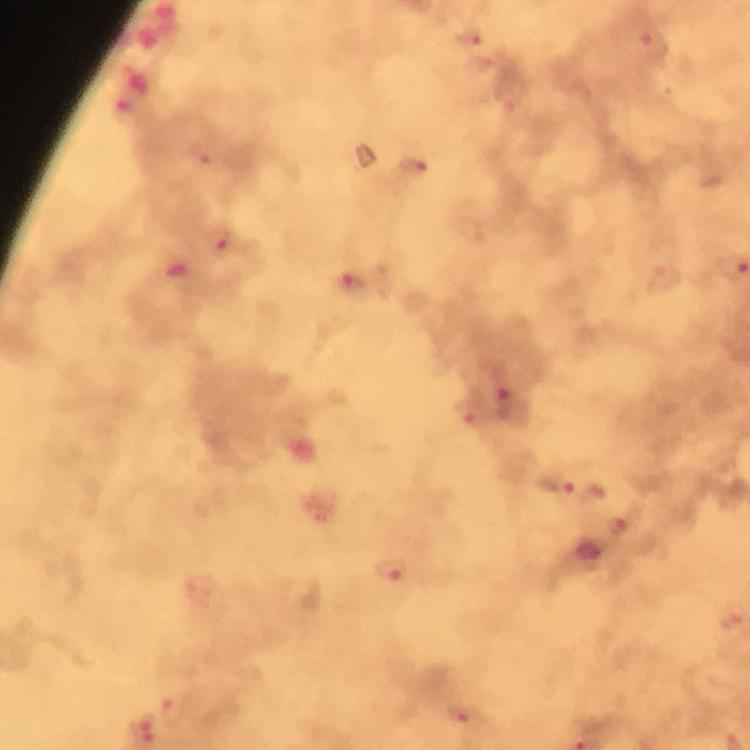

stain = Giemsa
cropped from = one field of view
capture = smartphone mounted on the microscope
Plasmodium parasite locations = approximate centers as [x, y] in pixels: [468, 36], [653, 44], [203, 154], [414, 167], [218, 241], [352, 282], [509, 403], [469, 411], [558, 485], [618, 528], [392, 569], [174, 710], [464, 713], [145, 730]
image size = 750×750 pixels
context = from a malaria diagnostic workup
magnification = 100x
immersion oil = used
preparation = thick blood smear